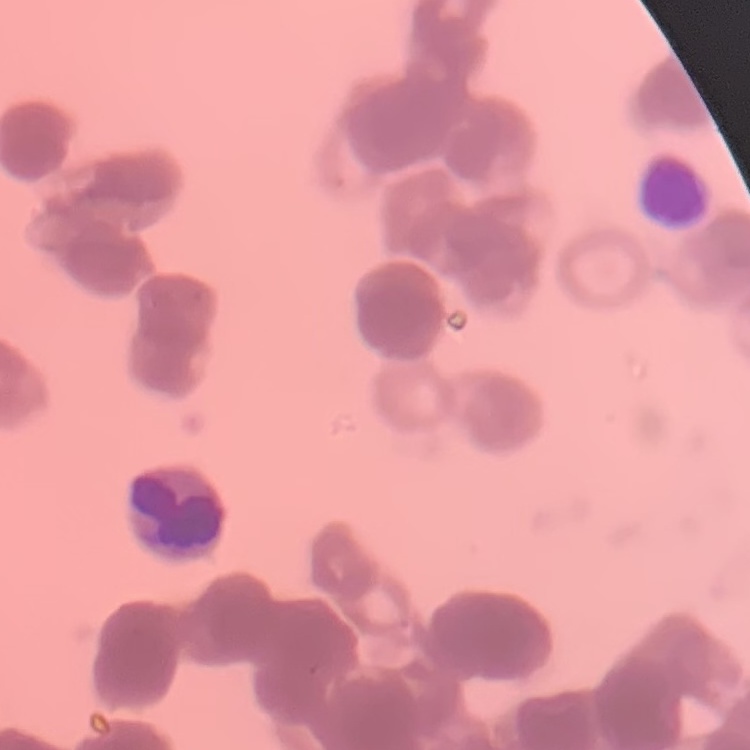
Summary:
  - Red blood cell morphology: rouleaux formation
  - Stain: Field's or Giemsa
  - Image type: square crop of a larger photomicrograph
  - Preparation: thin blood film